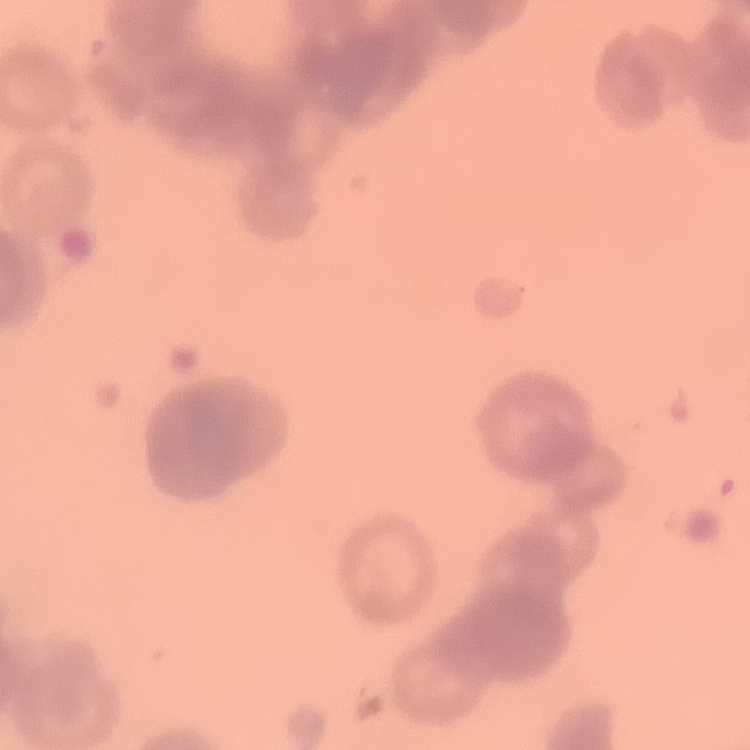

{
  "red_blood_cell_morphology": "rouleaux formation",
  "preparation": "thin blood film",
  "stain": "Field's or Giemsa",
  "image_type": "square crop of a larger photomicrograph"
}